Locate and identify every blood parasite.
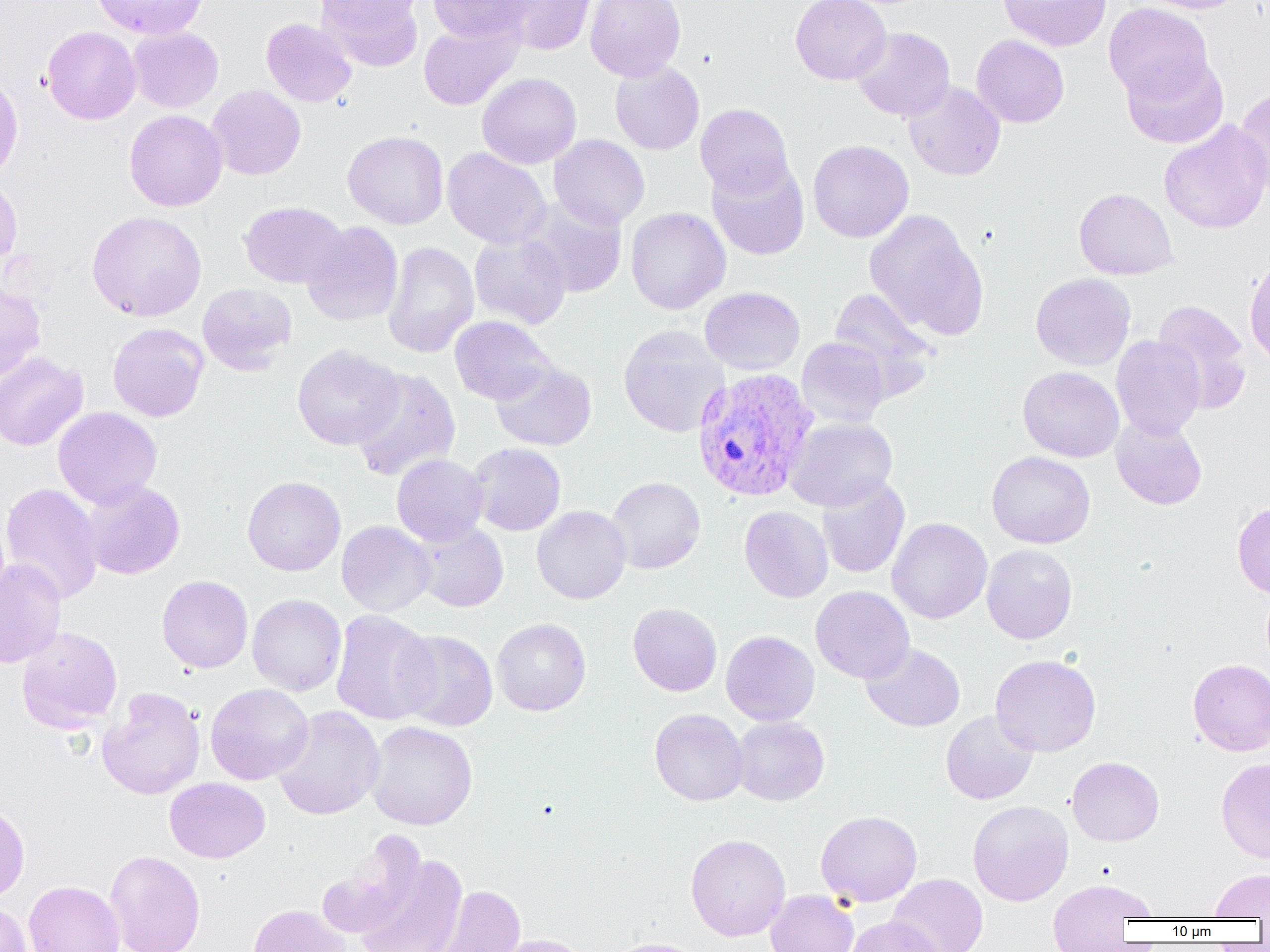

Approximate bounding boxes as [x1, y1, x2, y2] in pixels.
Plasmodium vivax-infected red blood cells: [692, 366, 819, 502].
No Plasmodium falciparum, Plasmodium ovale, Plasmodium malariae, Babesia divergens, or Trypanosoma brucei observed.

Uninfected red blood cell locations: [91, 0, 209, 39], [316, 0, 424, 70], [428, 0, 534, 44], [497, 0, 596, 55], [585, 0, 686, 81], [790, 0, 891, 85], [998, 0, 1111, 52], [1137, 0, 1247, 14], [315, 1, 426, 33], [1104, 3, 1214, 105], [261, 18, 357, 107], [419, 22, 521, 110], [42, 26, 141, 124], [128, 26, 223, 113], [852, 27, 955, 121], [971, 34, 1069, 128], [1121, 53, 1229, 149], [609, 61, 705, 155], [0, 71, 23, 184], [478, 72, 582, 169], [902, 81, 1005, 181], [206, 85, 306, 180], [1235, 87, 1270, 199], [695, 103, 794, 199], [124, 109, 227, 211], [1159, 119, 1270, 234], [343, 130, 449, 229], [549, 135, 649, 230], [807, 140, 914, 243], [442, 147, 551, 249], [707, 159, 809, 260], [0, 175, 22, 273], [1074, 188, 1178, 280], [520, 197, 628, 298], [239, 201, 347, 289], [626, 207, 730, 314], [864, 209, 989, 340], [87, 210, 207, 321], [302, 222, 403, 326], [470, 231, 571, 328], [383, 241, 479, 358], [1244, 257, 1270, 366], [1030, 273, 1136, 370], [0, 282, 45, 385], [197, 283, 297, 375], [700, 287, 805, 374], [829, 287, 936, 396], [1151, 300, 1252, 413], [450, 316, 555, 406], [107, 322, 209, 422], [618, 325, 728, 437], [1111, 335, 1205, 440], [797, 337, 890, 427], [292, 344, 403, 450], [0, 351, 89, 451], [491, 360, 596, 451], [1018, 366, 1124, 462], [350, 367, 461, 482], [53, 407, 162, 508], [1110, 416, 1207, 510], [784, 417, 897, 511], [467, 443, 566, 535], [987, 451, 1096, 549], [391, 454, 488, 546], [242, 475, 346, 576], [817, 475, 910, 579], [607, 477, 705, 574], [80, 480, 185, 579], [1, 482, 104, 605], [1233, 501, 1270, 597], [532, 506, 631, 604], [739, 506, 833, 603], [887, 517, 993, 624], [336, 520, 435, 616], [414, 521, 508, 612], [981, 544, 1078, 644], [0, 559, 66, 668], [157, 575, 253, 673], [811, 586, 914, 683], [247, 593, 346, 696], [628, 603, 722, 697], [330, 609, 439, 725], [491, 618, 591, 715], [17, 626, 123, 733], [392, 629, 498, 731], [721, 630, 820, 726], [861, 643, 965, 732], [990, 654, 1102, 757], [1188, 658, 1270, 755], [205, 683, 314, 785], [97, 686, 205, 800], [273, 706, 385, 820], [649, 708, 749, 805], [941, 710, 1038, 804], [732, 716, 829, 805], [366, 720, 478, 830], [1067, 756, 1164, 846], [1216, 758, 1270, 864], [164, 777, 270, 863], [0, 799, 30, 902], [968, 800, 1074, 906], [816, 810, 922, 907], [317, 833, 425, 940], [685, 833, 791, 941], [105, 849, 206, 952], [354, 849, 468, 952], [1209, 868, 1270, 920], [888, 873, 988, 952], [24, 881, 124, 952], [1047, 881, 1156, 951], [427, 884, 527, 952], [765, 889, 859, 952], [0, 901, 32, 952], [246, 904, 352, 952], [844, 915, 945, 952], [488, 934, 593, 952], [602, 937, 711, 952]. Slide-level diagnosis: Plasmodium vivax. Single field of view. 1000x magnification. Image is 1270×952 pixels. Optical microscopy. Thin blood film.